State which parasite is depicted.
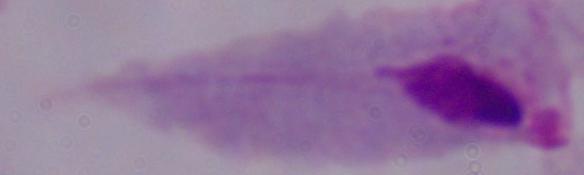
A trichomonad.

Captured at 1000x magnification. Micrograph.